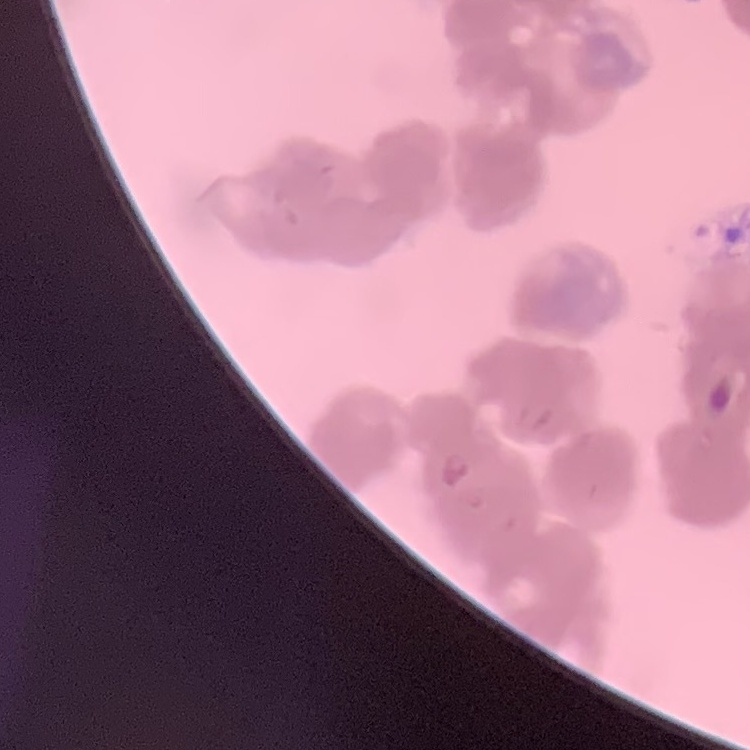
The erythrocytes exhibit rouleaux formation. One tile cut from a larger photomicrograph. Stained with either Field's or Giemsa. Thin peripheral smear.